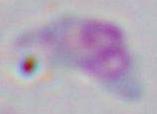

1000x magnification. Photomicrograph. Toxoplasma gondii is shown.